State the blood parasite species.
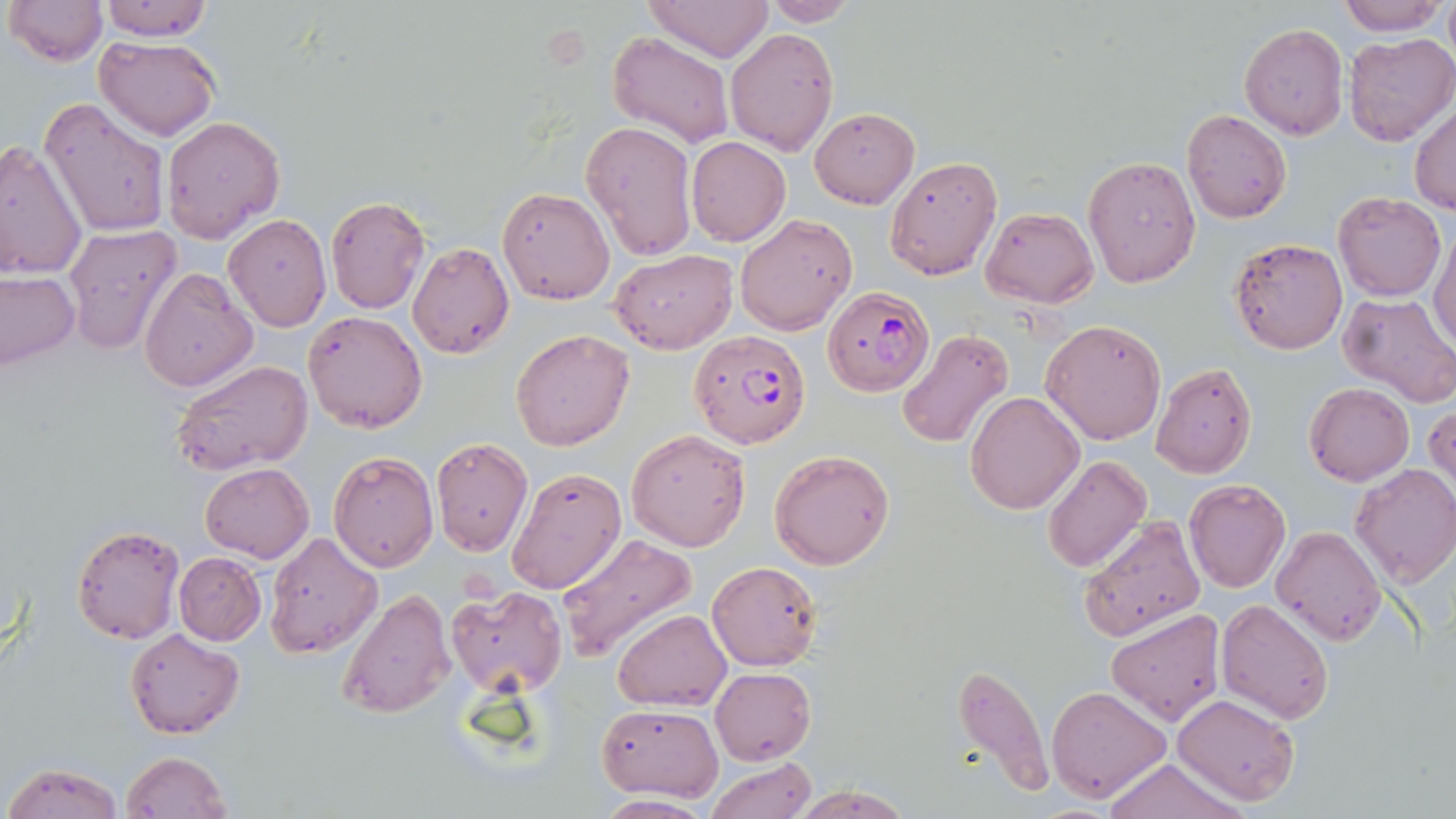

Plasmodium falciparum.

Summary:
  - Coordinate format: approximate bounding boxes as named x1/y1/x2/y2 corners in pixels
  - Plasmodium falciparum-infected red blood cell locations: (x1=821, y1=286, x2=935, y2=397), (x1=687, y1=329, x2=810, y2=449)
  - Uninfected red blood cell locations: (x1=4, y1=0, x2=105, y2=65), (x1=96, y1=0, x2=218, y2=41), (x1=645, y1=0, x2=771, y2=60), (x1=1336, y1=0, x2=1450, y2=37), (x1=758, y1=1, x2=860, y2=26), (x1=1239, y1=23, x2=1348, y2=139), (x1=724, y1=26, x2=839, y2=155), (x1=608, y1=31, x2=733, y2=147), (x1=1343, y1=32, x2=1456, y2=147), (x1=94, y1=35, x2=219, y2=140), (x1=39, y1=99, x2=171, y2=238), (x1=1410, y1=104, x2=1456, y2=216), (x1=809, y1=107, x2=919, y2=208), (x1=1182, y1=109, x2=1292, y2=224), (x1=162, y1=116, x2=285, y2=246), (x1=580, y1=120, x2=696, y2=261), (x1=686, y1=136, x2=791, y2=246), (x1=0, y1=139, x2=88, y2=283), (x1=884, y1=155, x2=1002, y2=281), (x1=1083, y1=156, x2=1200, y2=287), (x1=497, y1=187, x2=615, y2=304), (x1=1333, y1=192, x2=1445, y2=301), (x1=326, y1=196, x2=430, y2=314), (x1=979, y1=207, x2=1100, y2=309), (x1=224, y1=213, x2=331, y2=331), (x1=734, y1=213, x2=856, y2=336), (x1=63, y1=224, x2=182, y2=355), (x1=1430, y1=227, x2=1456, y2=350), (x1=1229, y1=237, x2=1347, y2=354), (x1=407, y1=240, x2=514, y2=360), (x1=610, y1=249, x2=738, y2=353), (x1=138, y1=266, x2=257, y2=392), (x1=0, y1=269, x2=81, y2=370), (x1=1336, y1=292, x2=1456, y2=410), (x1=303, y1=310, x2=426, y2=432), (x1=1040, y1=319, x2=1166, y2=445), (x1=511, y1=328, x2=635, y2=450), (x1=896, y1=329, x2=1016, y2=448), (x1=171, y1=358, x2=314, y2=477), (x1=1150, y1=364, x2=1256, y2=479), (x1=1304, y1=382, x2=1413, y2=485), (x1=965, y1=390, x2=1084, y2=514), (x1=1425, y1=400, x2=1455, y2=496), (x1=625, y1=428, x2=751, y2=552), (x1=430, y1=437, x2=533, y2=556), (x1=769, y1=449, x2=894, y2=570), (x1=329, y1=451, x2=439, y2=572), (x1=1043, y1=454, x2=1151, y2=573), (x1=1349, y1=463, x2=1456, y2=588), (x1=200, y1=464, x2=314, y2=562), (x1=506, y1=467, x2=628, y2=596), (x1=1185, y1=480, x2=1291, y2=593), (x1=1078, y1=515, x2=1204, y2=643), (x1=71, y1=525, x2=186, y2=645), (x1=1270, y1=525, x2=1385, y2=646), (x1=263, y1=532, x2=383, y2=658), (x1=555, y1=534, x2=698, y2=663), (x1=173, y1=552, x2=267, y2=644), (x1=706, y1=560, x2=822, y2=671), (x1=446, y1=584, x2=566, y2=693), (x1=337, y1=588, x2=453, y2=721), (x1=1215, y1=597, x2=1336, y2=724), (x1=612, y1=609, x2=730, y2=712), (x1=1103, y1=609, x2=1226, y2=728), (x1=125, y1=628, x2=244, y2=739), (x1=949, y1=661, x2=1055, y2=801), (x1=710, y1=666, x2=816, y2=764), (x1=1047, y1=684, x2=1172, y2=801), (x1=1173, y1=693, x2=1300, y2=808), (x1=595, y1=704, x2=723, y2=800), (x1=121, y1=750, x2=232, y2=818), (x1=706, y1=757, x2=817, y2=818), (x1=1102, y1=758, x2=1247, y2=819), (x1=3, y1=761, x2=124, y2=818), (x1=787, y1=784, x2=913, y2=818), (x1=593, y1=793, x2=712, y2=817)
  - Modality: optical microscopy
  - Image size: 1456×819 pixels
  - Preparation: thin blood film
  - Magnification: 1000x
  - Stain: May-Grünwald-Giemsa
  - Field of view: single